Assess this cell for malaria.
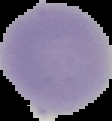
It is uninfected.

From a thin blood film. Segmented cell region on a black background. Image is 112×121 pixels.